Report the malaria status of this cell.
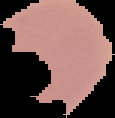
It is uninfected.

Cell region segmented out of the field of view; the surrounding area is masked to black. From a thin blood film. Image is 115×118 pixels.